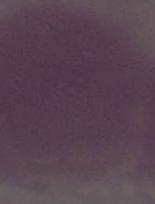

identification = red blood cell
magnification = 1000x
modality = micrograph